Classify this cell by malaria status.
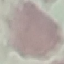
Uninfected.

Thin blood film. Acquired by smartphone through the microscope eyepiece. Cell patch, automatically extracted from a larger field of view and resized to 64 × 64 pixels. Giemsa-stained preparation.